Assess this cell for malaria.
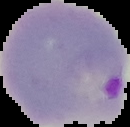

Parasitized.

From a thin blood smear. Segmented cell region on a black background. Image is 130×127 pixels.